Assess for malaria.
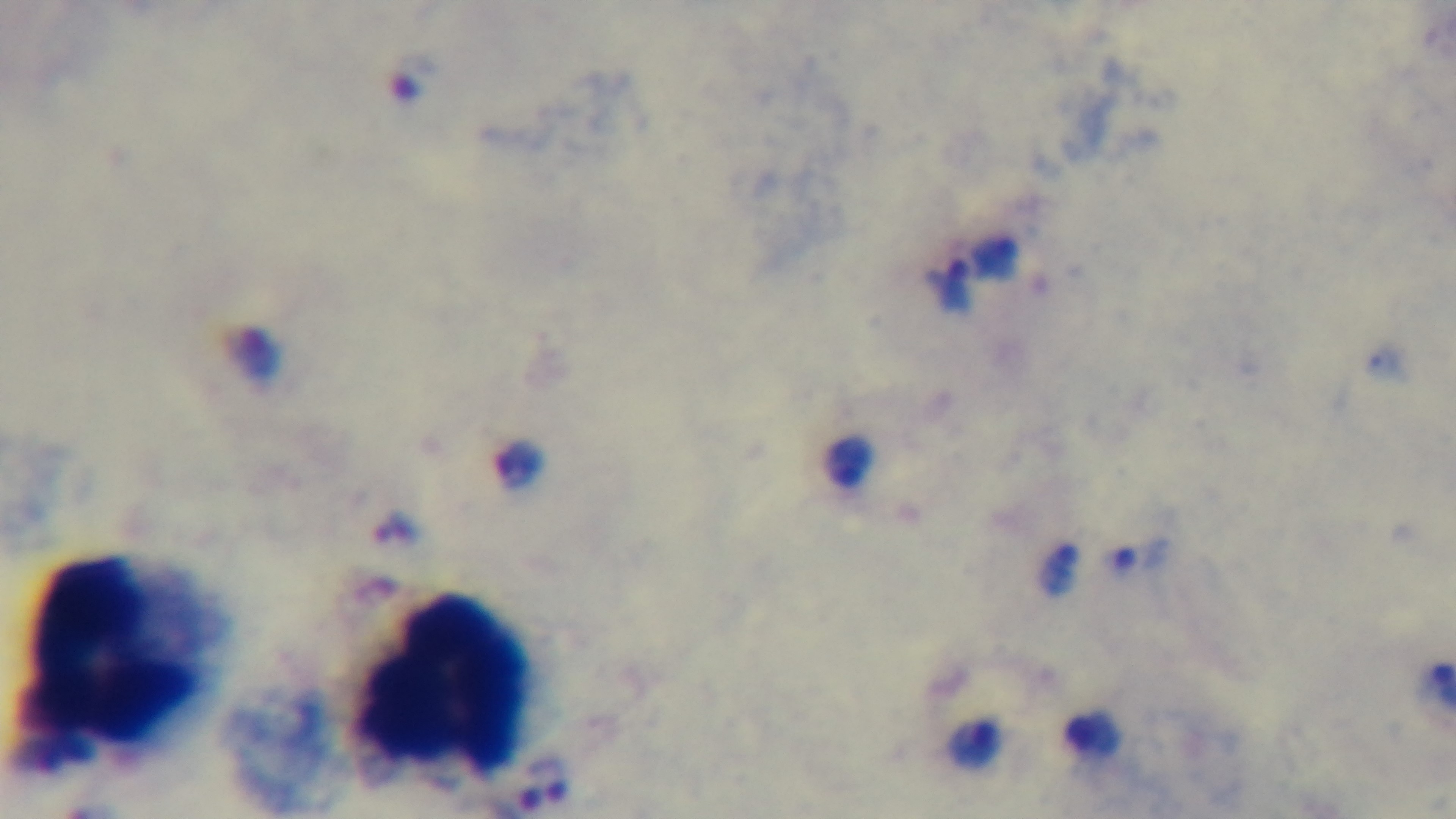

It is infected.

Giemsa-stained. Preparation: thick blood film. Captured with a mounted 4K digital camera. Light microscopy. 100x oil-immersion objective. One field from the slide.